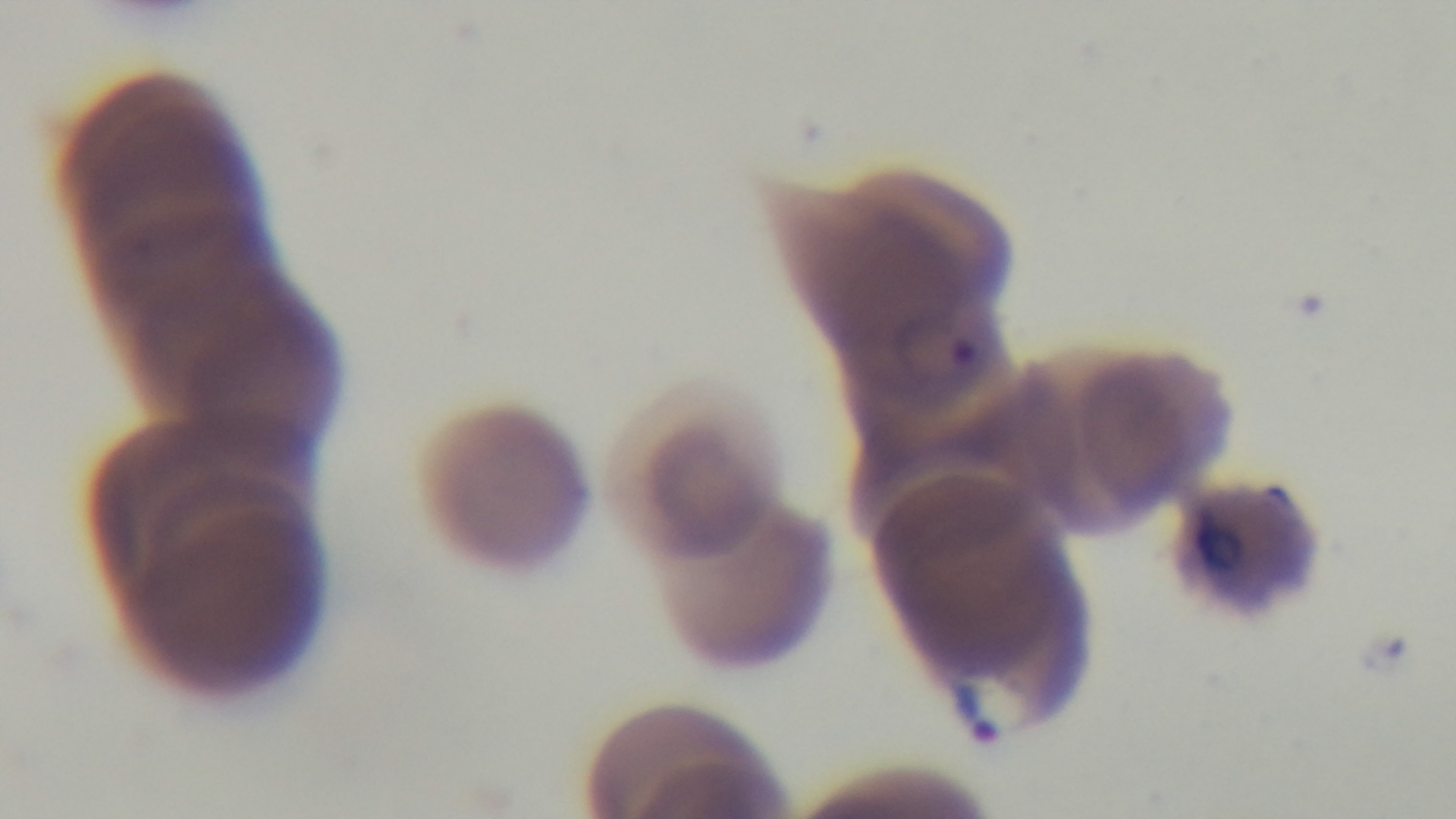
100x oil-immersion objective. Preparation: thin blood film. Mounted 4K digital camera. Single field of view. Malaria status: infected. Photomicrograph. Giemsa stain.